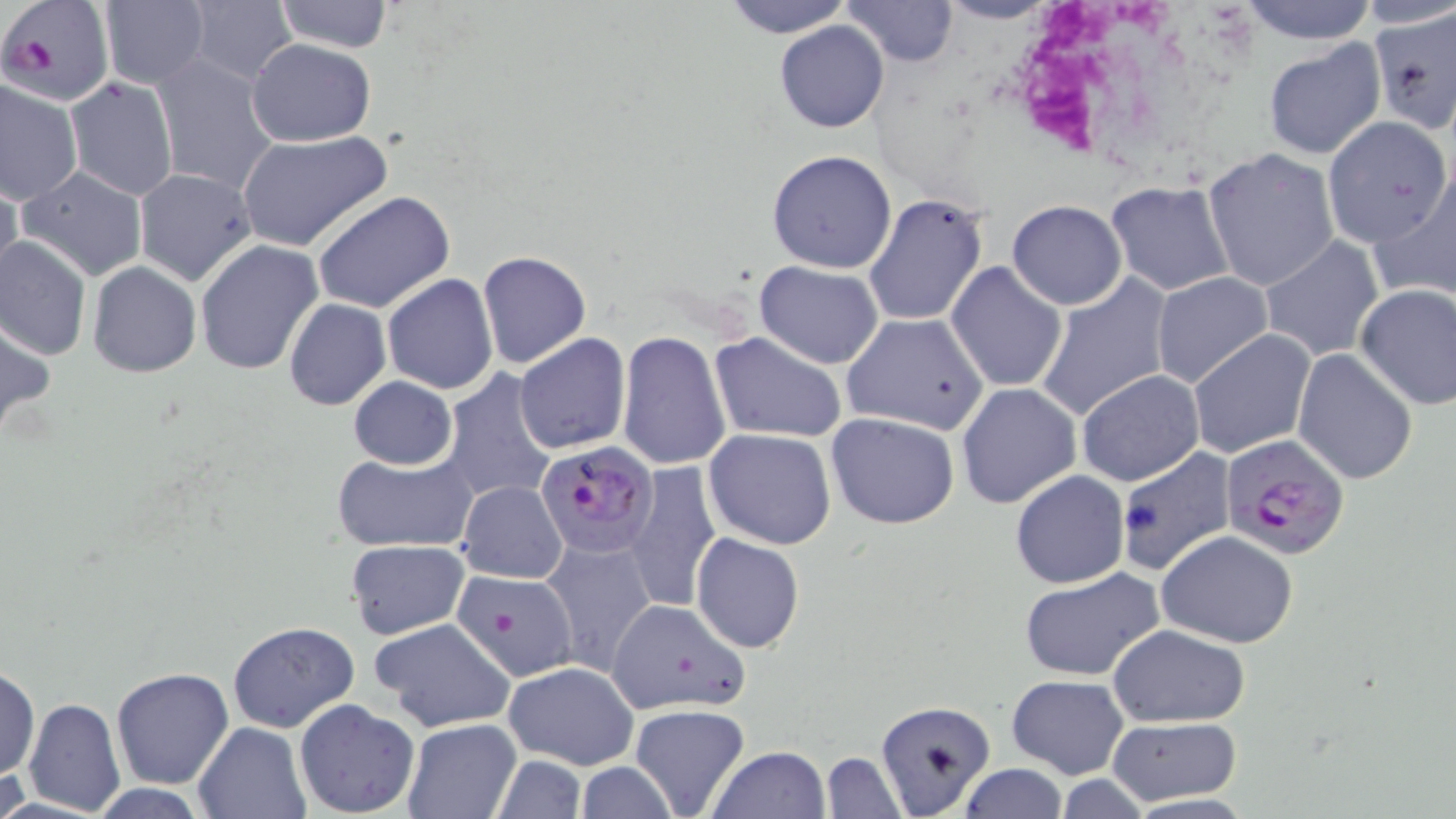

Summary:
  - Coordinate format: approximate bounding boxes as (x1, y1, x2, y2) in pixels
  - Uninfected red blood cell locations: (98, 0, 210, 89), (271, 0, 395, 53), (724, 0, 850, 38), (844, 0, 958, 67), (936, 0, 1062, 24), (1238, 0, 1378, 43), (1354, 0, 1456, 30), (185, 2, 297, 85), (1366, 13, 1455, 134), (774, 21, 889, 132), (247, 38, 376, 146), (1263, 39, 1386, 159), (151, 56, 278, 197), (0, 73, 83, 206), (64, 76, 178, 200), (1322, 117, 1453, 250), (235, 130, 393, 252), (766, 149, 898, 273), (1202, 149, 1339, 292), (16, 165, 148, 282), (134, 167, 256, 285), (1371, 169, 1456, 306), (0, 172, 23, 295), (1106, 181, 1238, 297), (313, 192, 456, 314), (862, 195, 989, 327), (1008, 199, 1127, 309), (0, 234, 90, 361), (1258, 236, 1386, 361), (195, 240, 324, 376), (477, 251, 590, 368), (755, 260, 884, 368), (946, 260, 1069, 393), (87, 261, 201, 379), (1150, 270, 1273, 390), (382, 272, 498, 395), (1031, 274, 1173, 423), (1354, 283, 1456, 411), (283, 298, 390, 411), (840, 312, 990, 435), (1, 316, 53, 440), (1187, 330, 1315, 461), (617, 331, 733, 471), (710, 332, 847, 443), (515, 333, 632, 455), (1292, 348, 1419, 485), (439, 369, 557, 504), (1076, 370, 1204, 487), (349, 376, 457, 470), (956, 381, 1081, 508), (827, 412, 960, 529), (705, 427, 837, 549), (1115, 446, 1237, 576), (333, 451, 478, 554), (623, 462, 720, 615), (1010, 470, 1128, 588), (456, 479, 569, 585), (1156, 529, 1299, 647), (691, 532, 805, 653), (543, 533, 660, 672), (345, 540, 469, 640), (1020, 566, 1165, 682), (451, 568, 582, 685), (604, 598, 751, 714), (371, 616, 515, 733), (228, 621, 361, 735), (1109, 624, 1250, 727), (503, 661, 639, 770), (1, 662, 40, 782), (110, 666, 234, 789), (1008, 674, 1128, 779), (23, 698, 126, 816), (294, 699, 421, 817), (873, 700, 996, 817), (628, 703, 751, 819), (1106, 715, 1242, 806), (402, 719, 522, 818), (191, 721, 310, 818), (706, 746, 832, 819), (820, 752, 903, 818), (491, 757, 586, 817), (576, 762, 678, 818), (958, 763, 1069, 818), (1054, 775, 1155, 817), (1121, 795, 1258, 818)
  - Plasmodium falciparum-infected red blood cell locations: (2, 0, 112, 104), (1222, 437, 1348, 561), (522, 444, 661, 562)
  - White blood cell locations: (1014, 0, 1216, 162)
  - Slide-level diagnosis: Plasmodium falciparum
  - Field of view: single
  - Preparation: thin blood film
  - Magnification: 1000x
  - Modality: light microscopy
  - Image size: 1456×819 pixels
  - Stain: May-Grünwald-Giemsa